Locate and identify every blood parasite.
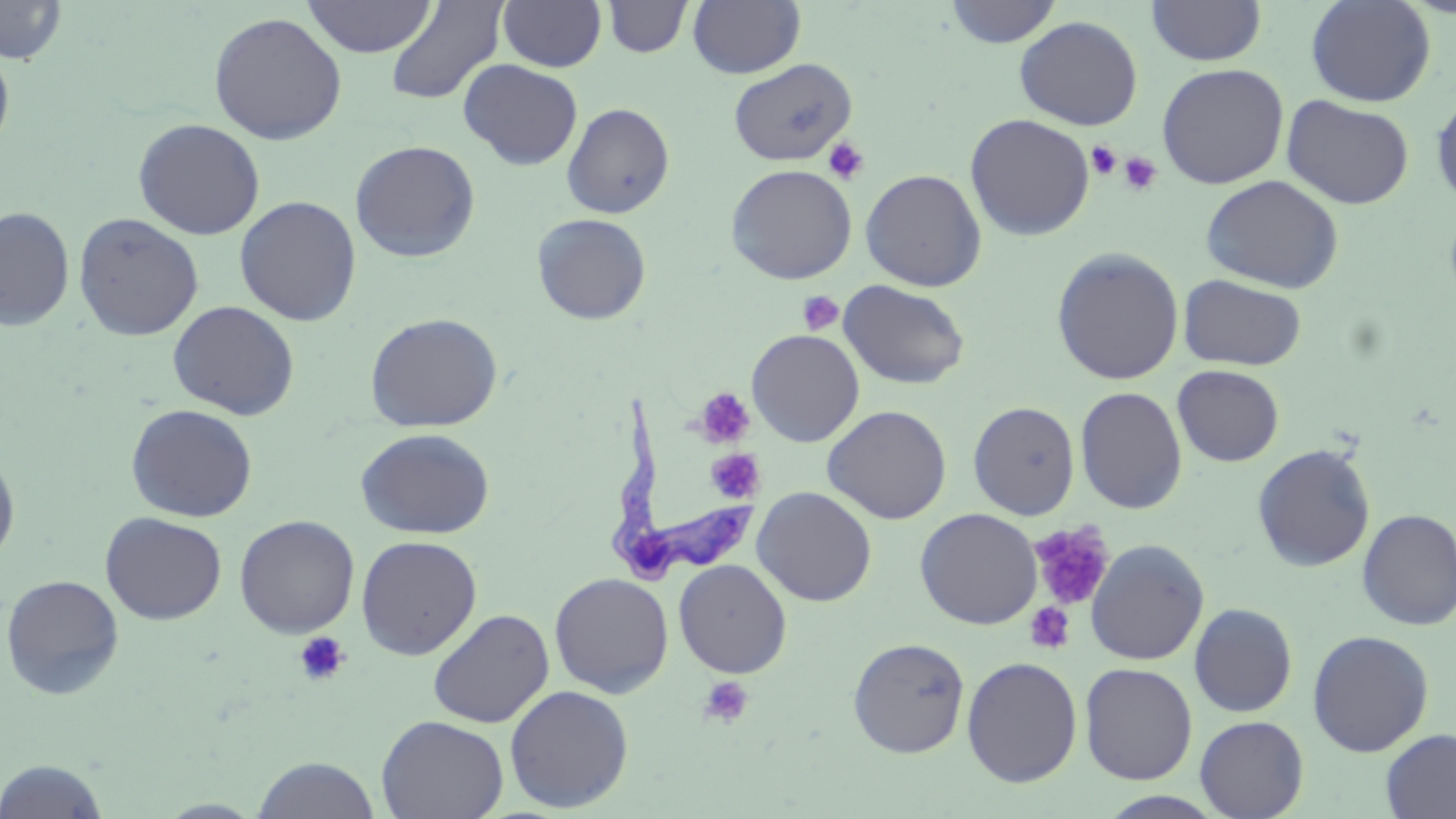

Approximate bounding boxes as named x1/y1/x2/y2 corners in pixels.
Trypanosoma brucei: (x1=606, y1=394, x2=761, y2=584).
No Plasmodium falciparum, Plasmodium ovale, Plasmodium malariae, Plasmodium vivax, or Babesia divergens observed.

Summary:
  - Platelet locations: (x1=823, y1=137, x2=869, y2=185), (x1=1086, y1=141, x2=1122, y2=181), (x1=1117, y1=151, x2=1163, y2=196), (x1=797, y1=290, x2=844, y2=336), (x1=694, y1=387, x2=756, y2=448), (x1=706, y1=448, x2=767, y2=504), (x1=1028, y1=521, x2=1115, y2=612), (x1=1024, y1=601, x2=1076, y2=655), (x1=292, y1=630, x2=350, y2=686), (x1=697, y1=675, x2=755, y2=729)
  - Uninfected red blood cell locations: (x1=302, y1=0, x2=437, y2=58), (x1=498, y1=0, x2=607, y2=72), (x1=602, y1=0, x2=693, y2=58), (x1=688, y1=0, x2=805, y2=78), (x1=945, y1=0, x2=1062, y2=47), (x1=1305, y1=0, x2=1436, y2=107), (x1=0, y1=1, x2=67, y2=65), (x1=385, y1=1, x2=507, y2=106), (x1=1146, y1=1, x2=1266, y2=66), (x1=208, y1=11, x2=347, y2=145), (x1=1014, y1=15, x2=1143, y2=130), (x1=0, y1=44, x2=15, y2=157), (x1=729, y1=58, x2=856, y2=167), (x1=458, y1=59, x2=583, y2=170), (x1=1156, y1=62, x2=1289, y2=189), (x1=1430, y1=91, x2=1456, y2=209), (x1=1281, y1=95, x2=1415, y2=209), (x1=561, y1=102, x2=675, y2=218), (x1=965, y1=113, x2=1095, y2=240), (x1=132, y1=118, x2=266, y2=240), (x1=349, y1=140, x2=481, y2=263), (x1=726, y1=163, x2=857, y2=284), (x1=860, y1=169, x2=987, y2=292), (x1=1200, y1=174, x2=1344, y2=293), (x1=234, y1=195, x2=361, y2=326), (x1=0, y1=206, x2=75, y2=331), (x1=73, y1=213, x2=204, y2=341), (x1=532, y1=213, x2=651, y2=325), (x1=1051, y1=247, x2=1184, y2=385), (x1=1178, y1=274, x2=1307, y2=371), (x1=838, y1=279, x2=971, y2=390), (x1=167, y1=300, x2=300, y2=420), (x1=365, y1=312, x2=503, y2=432), (x1=746, y1=328, x2=865, y2=447), (x1=1172, y1=364, x2=1284, y2=467), (x1=1075, y1=386, x2=1188, y2=514), (x1=968, y1=401, x2=1080, y2=519), (x1=126, y1=403, x2=257, y2=523), (x1=822, y1=405, x2=952, y2=524), (x1=356, y1=427, x2=495, y2=539), (x1=1252, y1=443, x2=1376, y2=572), (x1=0, y1=451, x2=20, y2=568), (x1=753, y1=486, x2=877, y2=606), (x1=915, y1=508, x2=1042, y2=629), (x1=1356, y1=508, x2=1456, y2=631), (x1=100, y1=512, x2=226, y2=625), (x1=234, y1=515, x2=360, y2=638), (x1=356, y1=535, x2=482, y2=660), (x1=1084, y1=539, x2=1209, y2=665), (x1=673, y1=559, x2=792, y2=678), (x1=549, y1=572, x2=674, y2=697), (x1=1, y1=574, x2=125, y2=700), (x1=1188, y1=603, x2=1297, y2=717), (x1=428, y1=609, x2=554, y2=728), (x1=1307, y1=630, x2=1434, y2=756), (x1=848, y1=637, x2=970, y2=757), (x1=961, y1=656, x2=1083, y2=787), (x1=1079, y1=662, x2=1198, y2=785), (x1=504, y1=684, x2=634, y2=813), (x1=376, y1=715, x2=509, y2=819), (x1=1195, y1=715, x2=1308, y2=819), (x1=1380, y1=728, x2=1456, y2=819), (x1=251, y1=756, x2=382, y2=818), (x1=0, y1=759, x2=112, y2=819), (x1=1097, y1=791, x2=1228, y2=818)
  - Slide-level diagnosis: Trypanosoma brucei
  - Stain: May-Grünwald-Giemsa
  - Magnification: 1000x
  - Field of view: single
  - Modality: light microscopy
  - Preparation: thin blood film
  - Image size: 1456×819 pixels